Evaluate for Plasmodium parasites.
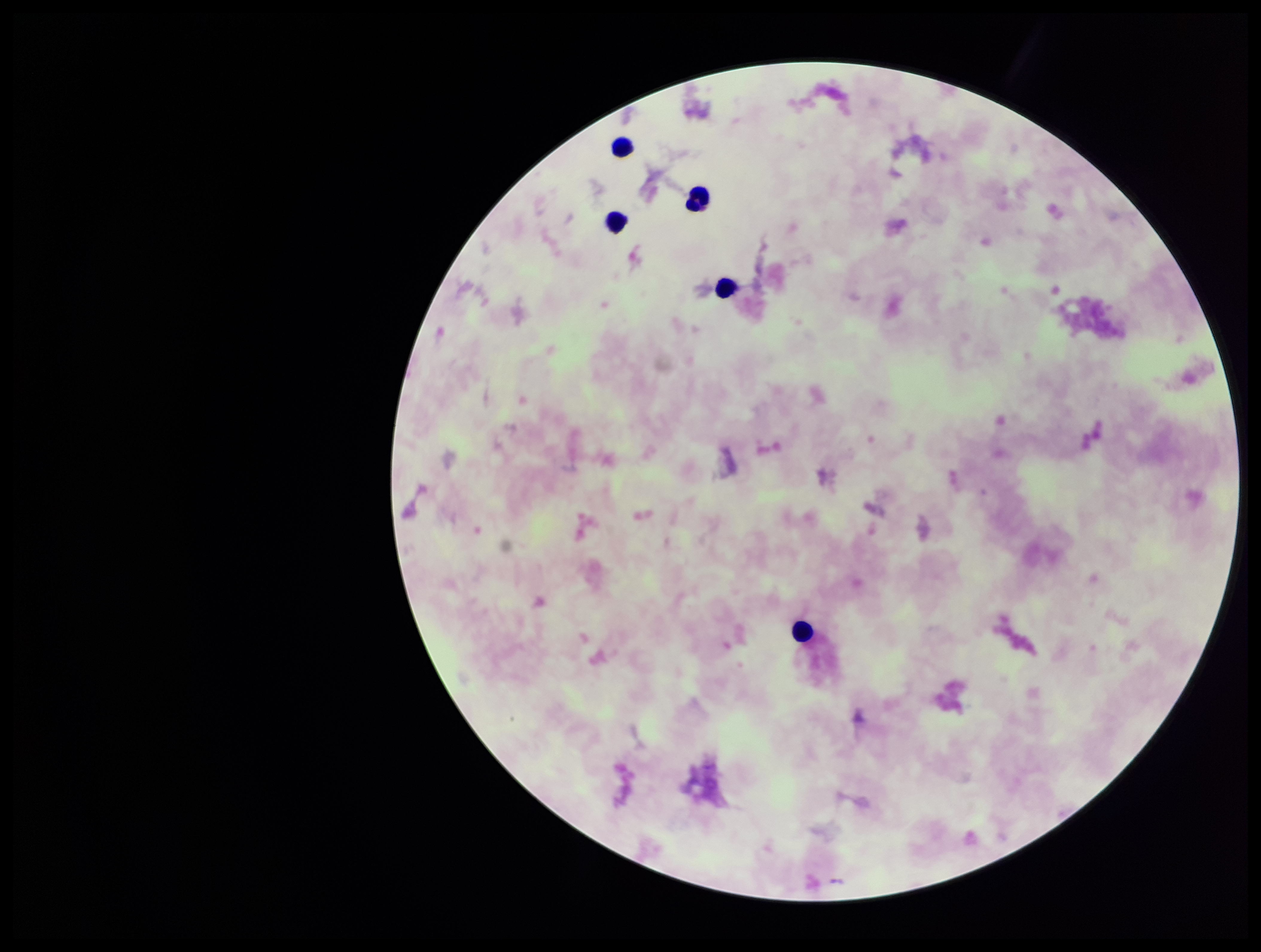

None detected.

stain = Giemsa
field of view = single
capture = smartphone photograph through the microscope eyepiece
preparation = thick smear
parasite count = 0
image size = 1261×952 pixels
leukocyte count = 5
patient malaria status = negative